Give the preparation type.
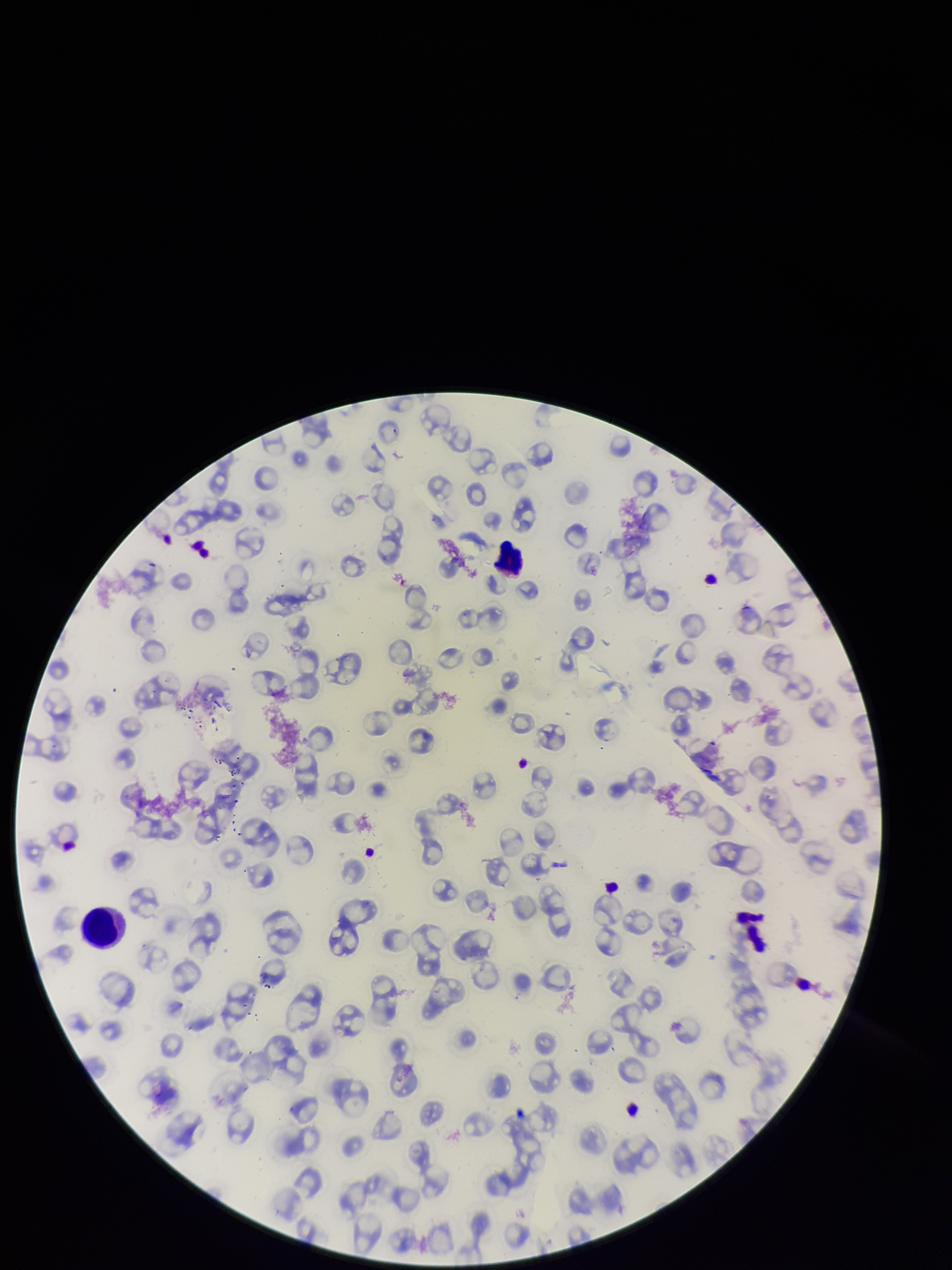
Thin.

One field from this slide. Parasitized red blood cell count: 0. Red blood cell count: 88. Giemsa stain. Patient malaria status: positive. Smartphone photograph taken through the eyepiece of a microscope. Image is 952×1270 pixels. Parasitized red blood cells: none detected. Species reported for this patient: Plasmodium falciparum.